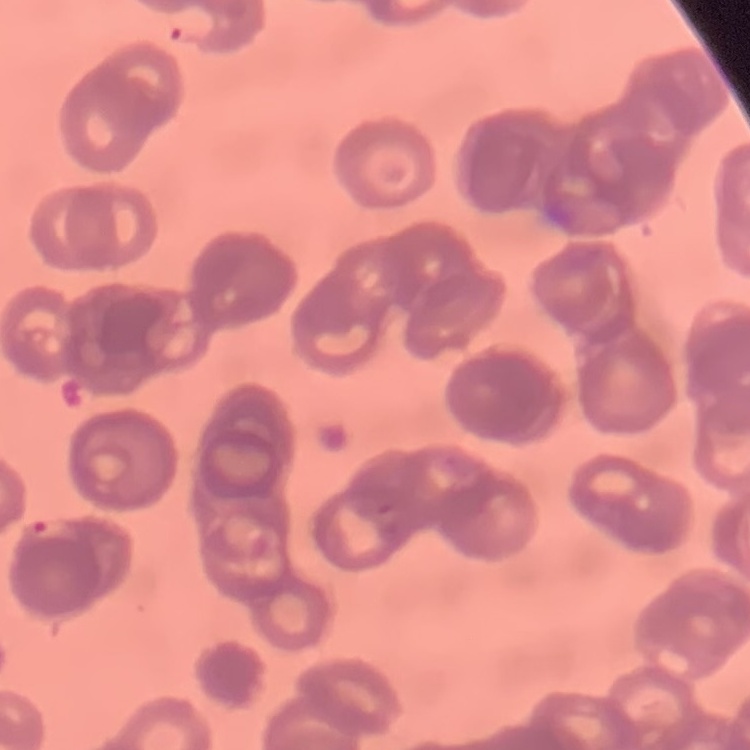

{
  "erythrocyte_morphology": "rouleaux formation",
  "image_type": "square crop of a larger photomicrograph",
  "stain": "Field's or Giemsa",
  "preparation": "thin peripheral smear"
}